State which parasite is depicted.
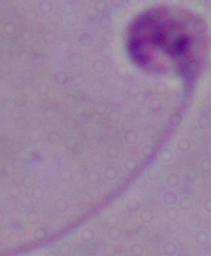
Leishmania.

Summary:
  - Magnification: 1000x
  - Modality: photomicrograph